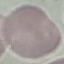

Summary:
  - Malaria status: uninfected
  - Image type: cell patch, automatically extracted from a larger field of view and resized to 64 × 64 pixels
  - Preparation: thin blood film
  - Capture: smartphone camera at the microscope eyepiece
  - Stain: Giemsa